Identify the parasite.
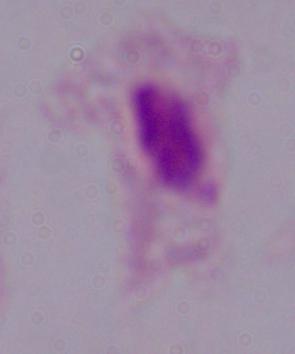

This is a trichomonad.

Summary:
  - Modality: photomicrograph
  - Magnification: 1000x